Name the parasite shown.
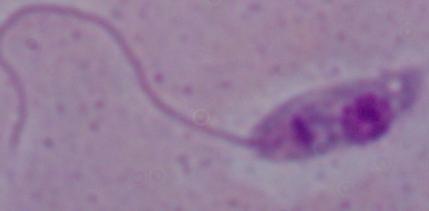
Leishmania.

1000x magnification. Photomicrograph.